Identify the cell.
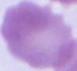

An erythrocyte.

Captured at 1000x magnification. Micrograph.